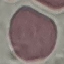
Summary:
  - Malaria status: uninfected
  - Stain: Giemsa
  - Image type: cell patch, automatically extracted from a larger field of view and resized to 64 × 64 pixels
  - Capture: smartphone camera at the microscope eyepiece
  - Preparation: thin blood film